Locate the cells, classifying each as a parasitized RBC, an uninfected RBC, or a WBC.
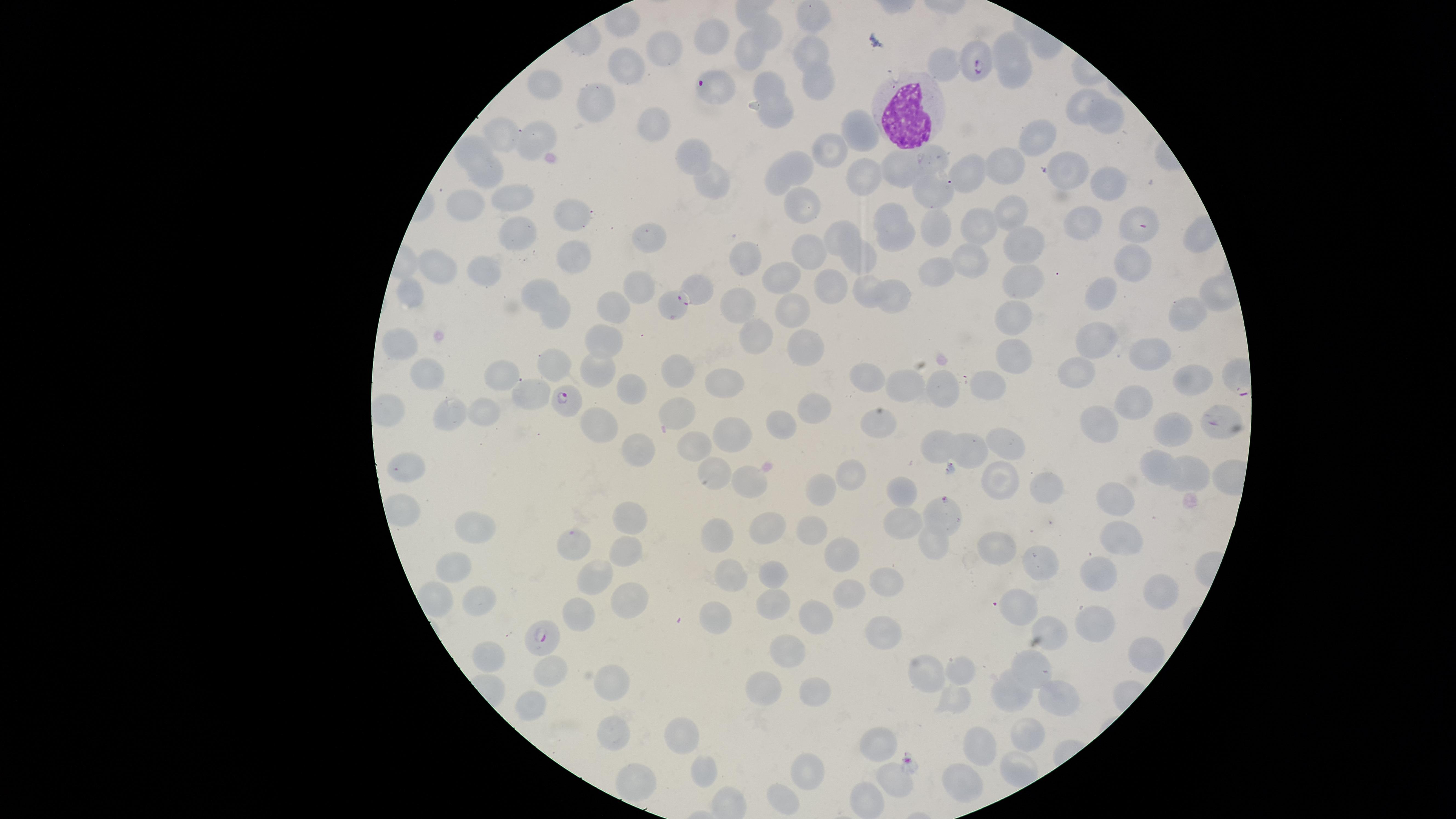

Approximate marker points as {x, y} in pixels.
Parasitized RBCs: {976, 62}, {706, 86}, {696, 291}, {569, 399}, {943, 510}, {546, 636}.
Uninfected RBCs: {712, 32}, {765, 32}, {663, 44}, {1011, 45}, {816, 49}, {749, 53}, {627, 64}, {946, 72}, {1012, 75}, {818, 80}, {549, 83}, {773, 85}, {598, 104}, {1080, 107}, {780, 117}, {1111, 118}, {656, 124}, {508, 133}, {536, 134}, {1036, 134}, {860, 135}, {477, 146}, {697, 151}, {836, 152}, {936, 159}, {908, 163}, {1007, 164}, {805, 165}, {1066, 165}, {969, 166}, {487, 176}, {866, 177}, {713, 180}, {778, 182}, {1104, 185}, {931, 192}, {519, 200}, {469, 201}, {1013, 209}, {802, 211}, {569, 212}, {893, 213}, {1142, 219}, {941, 227}, {982, 228}, {1083, 229}, {515, 233}, {842, 235}, {647, 239}, {1021, 243}, {899, 244}, {809, 248}, {579, 253}, {746, 255}, {860, 257}, {442, 261}, {974, 263}, {1132, 264}, {488, 266}, {943, 269}, {1023, 277}, {869, 281}, {782, 283}, {640, 285}, {540, 287}, {835, 287}, {414, 294}, {1100, 294}, {895, 298}, {744, 302}, {617, 304}, {670, 306}, {1018, 313}, {794, 314}, {557, 315}, {1188, 315}, {605, 335}, {751, 336}, {1093, 343}, {401, 345}, {807, 345}, {1147, 351}, {1018, 355}, {562, 357}, {504, 369}, {676, 370}, {596, 372}, {869, 373}, {431, 374}, {1078, 374}, {1190, 378}, {724, 381}, {909, 383}, {947, 383}, {637, 388}, {988, 389}, {533, 394}, {818, 403}, {1135, 406}, {677, 409}, {486, 411}, {444, 413}, {1211, 416}, {1101, 421}, {1170, 425}, {603, 426}, {879, 428}, {776, 432}, {734, 436}, {1007, 439}, {932, 444}, {690, 446}, {970, 451}, {637, 454}, {1161, 461}, {411, 463}, {717, 473}, {848, 476}, {1003, 479}, {1195, 479}, {757, 488}, {1042, 489}, {825, 490}, {1121, 493}, {904, 497}, {631, 512}, {898, 519}, {476, 526}, {768, 529}, {815, 530}, {717, 533}, {1123, 536}, {932, 543}, {580, 545}, {995, 548}, {628, 551}, {848, 554}, {1033, 559}, {458, 565}, {1104, 569}, {598, 576}, {773, 576}, {734, 577}, {885, 583}, {849, 591}, {623, 596}, {478, 598}, {1151, 599}, {774, 600}, {436, 601}, {1018, 608}, {581, 610}, {717, 617}, {817, 618}, {1096, 620}, {1050, 627}, {876, 630}, {793, 647}, {1144, 650}, {493, 659}, {1031, 665}, {963, 670}, {557, 675}, {926, 678}, {761, 680}, {616, 684}, {1013, 693}, {812, 694}, {1057, 697}, {957, 699}, {533, 704}, {615, 723}, {1028, 735}, {686, 744}, {883, 745}, {981, 745}, {805, 765}, {705, 772}, {644, 777}, {966, 781}, {895, 782}, {786, 799}, {864, 804}.
WBCs: {905, 116}.

Summary:
  - Species: Plasmodium falciparum
  - Preparation: thin blood film
  - Field of view: single
  - Stain: Giemsa
  - Image size: 1456×819 pixels
  - Visible region: circular
  - Capture: smartphone photograph through the microscope eyepiece